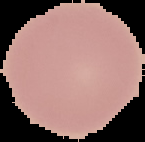

result = negative for Plasmodium parasites
preparation = thin blood film
image type = segmented cell region with the area outside set to black
image size = 145×142 pixels